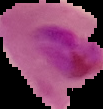

result = Plasmodium parasites detected
image size = 103×109 pixels
preparation = thin blood smear
image type = cell region segmented out of the field of view; surrounding area masked to black